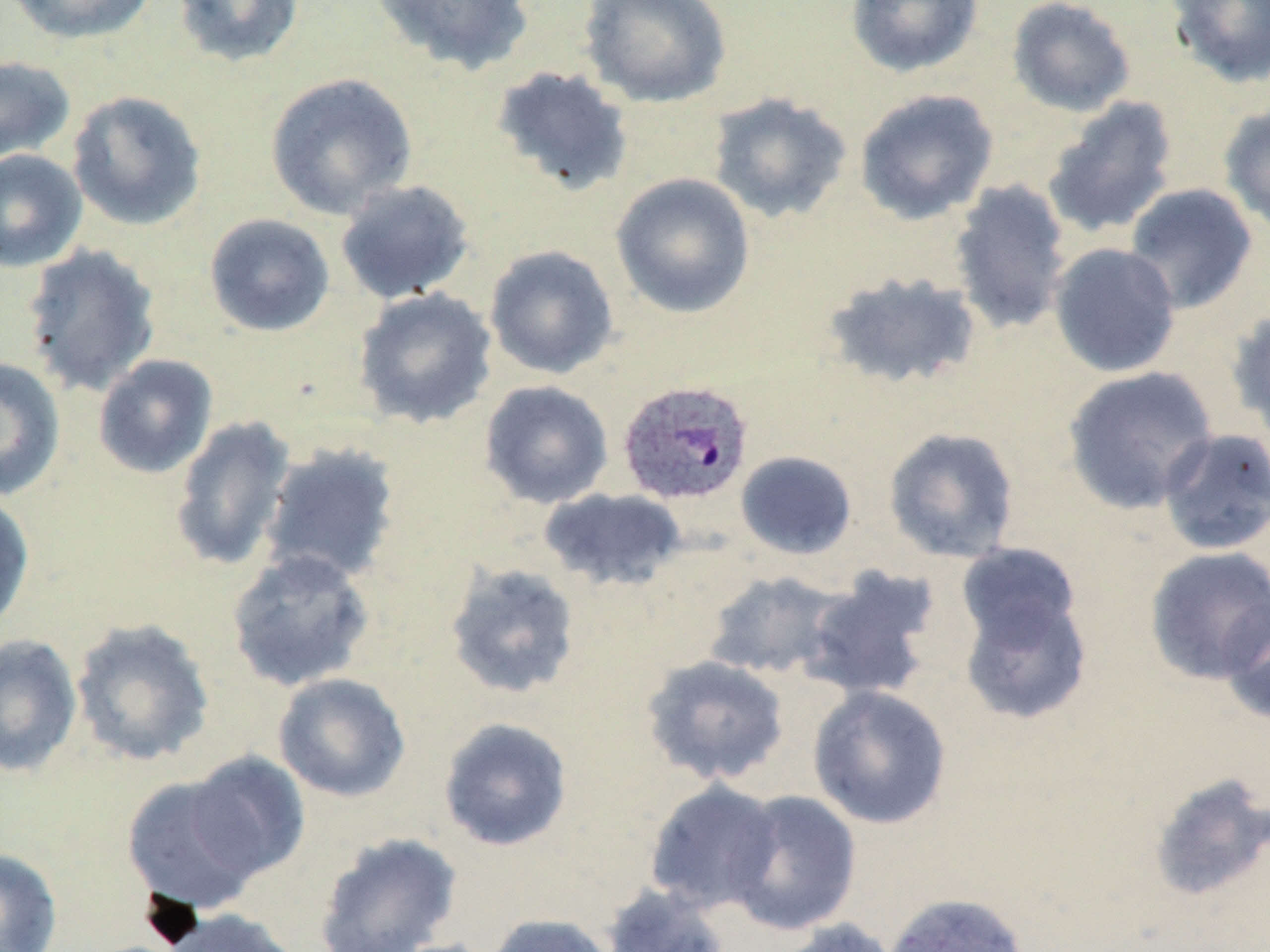
Summary:
  - Coordinate format: approximate bounding boxes as (x1,y1)-(x2,y2) corner pairs in pixels
  - Plasmodium ovale-infected red blood cell locations: (616,379)-(754,507)
  - Uninfected red blood cell locations: (5,0)-(158,45), (171,0)-(306,68), (371,0)-(536,76), (579,0)-(731,108), (845,0)-(985,78), (1007,0)-(1136,118), (1168,0)-(1270,89), (0,55)-(77,165), (491,65)-(634,197), (265,72)-(418,219), (854,88)-(999,225), (66,90)-(207,231), (708,92)-(853,224), (1042,96)-(1179,239), (1218,102)-(1270,236), (0,148)-(88,273), (610,172)-(755,319), (947,179)-(1074,336), (334,180)-(475,304), (1124,183)-(1259,314), (203,213)-(336,337), (21,243)-(162,397), (1049,243)-(1181,378), (484,245)-(619,380), (821,270)-(984,392), (352,287)-(498,430), (1227,308)-(1270,445), (93,354)-(218,479), (0,357)-(66,501), (1061,365)-(1219,515), (479,380)-(614,509), (169,414)-(297,573), (883,427)-(1019,563), (1157,427)-(1270,556), (259,441)-(402,586), (735,450)-(858,560), (538,487)-(687,593), (0,490)-(35,635), (956,543)-(1084,651), (1143,547)-(1270,685), (225,548)-(376,692), (443,561)-(583,701), (797,565)-(943,701), (701,570)-(844,680), (958,588)-(1092,725), (1219,595)-(1270,727), (69,617)-(216,768), (0,634)-(83,779), (640,654)-(791,787), (273,672)-(411,802), (807,685)-(952,830), (438,717)-(573,852), (184,750)-(312,882), (1148,772)-(1270,902), (121,774)-(266,915), (643,779)-(784,915), (725,790)-(861,936), (313,832)-(463,952), (0,847)-(63,952), (600,884)-(732,952), (881,892)-(1029,952), (154,907)-(305,952), (483,913)-(618,952), (773,918)-(901,952)
  - Slide-level diagnosis: Plasmodium ovale
  - Field of view: single
  - Image size: 1270×952 pixels
  - Modality: optical microscopy
  - Stain: May-Grünwald-Giemsa
  - Preparation: thin blood film
  - Magnification: 1000x